Comment on the morphology of the erythrocytes.
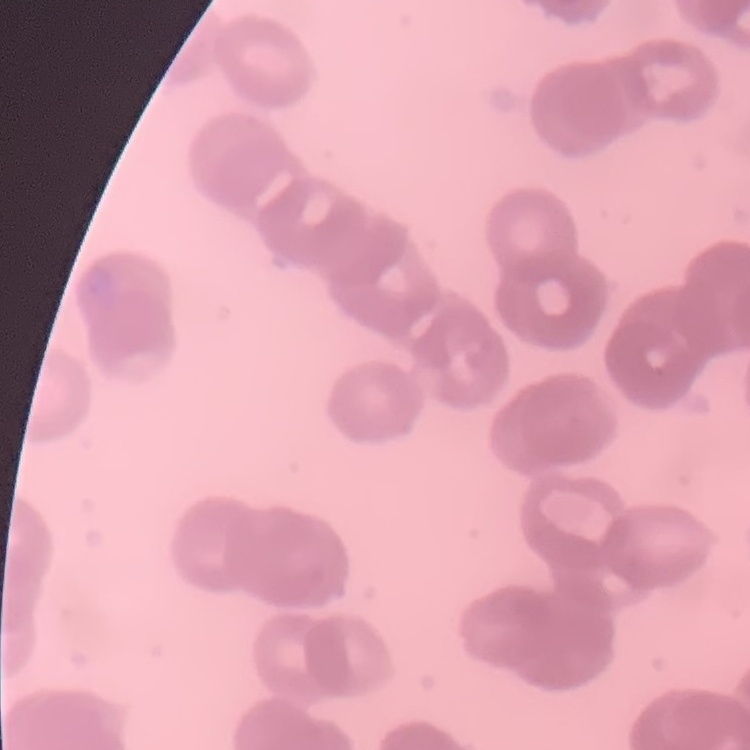

Rouleaux formation.

Field's or Giemsa stain. Square crop of a larger photomicrograph. Thin blood smear.